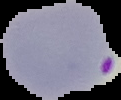
image_size: 121×100 pixels
image_type: segmented cell region with the area outside set to black
malaria_status: parasitized
preparation: thin blood smear